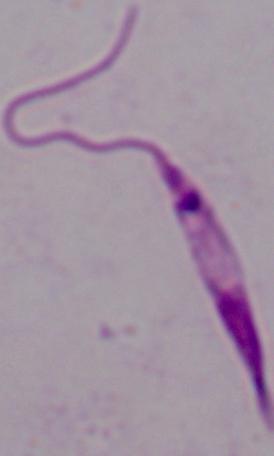
Summary:
  - Modality: micrograph
  - Identification: Leishmania
  - Magnification: 1000x